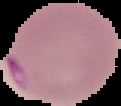

malaria status = parasitized
preparation = thin blood film
image size = 121×106 pixels
image type = cell region segmented out of the field of view; surrounding area masked to black